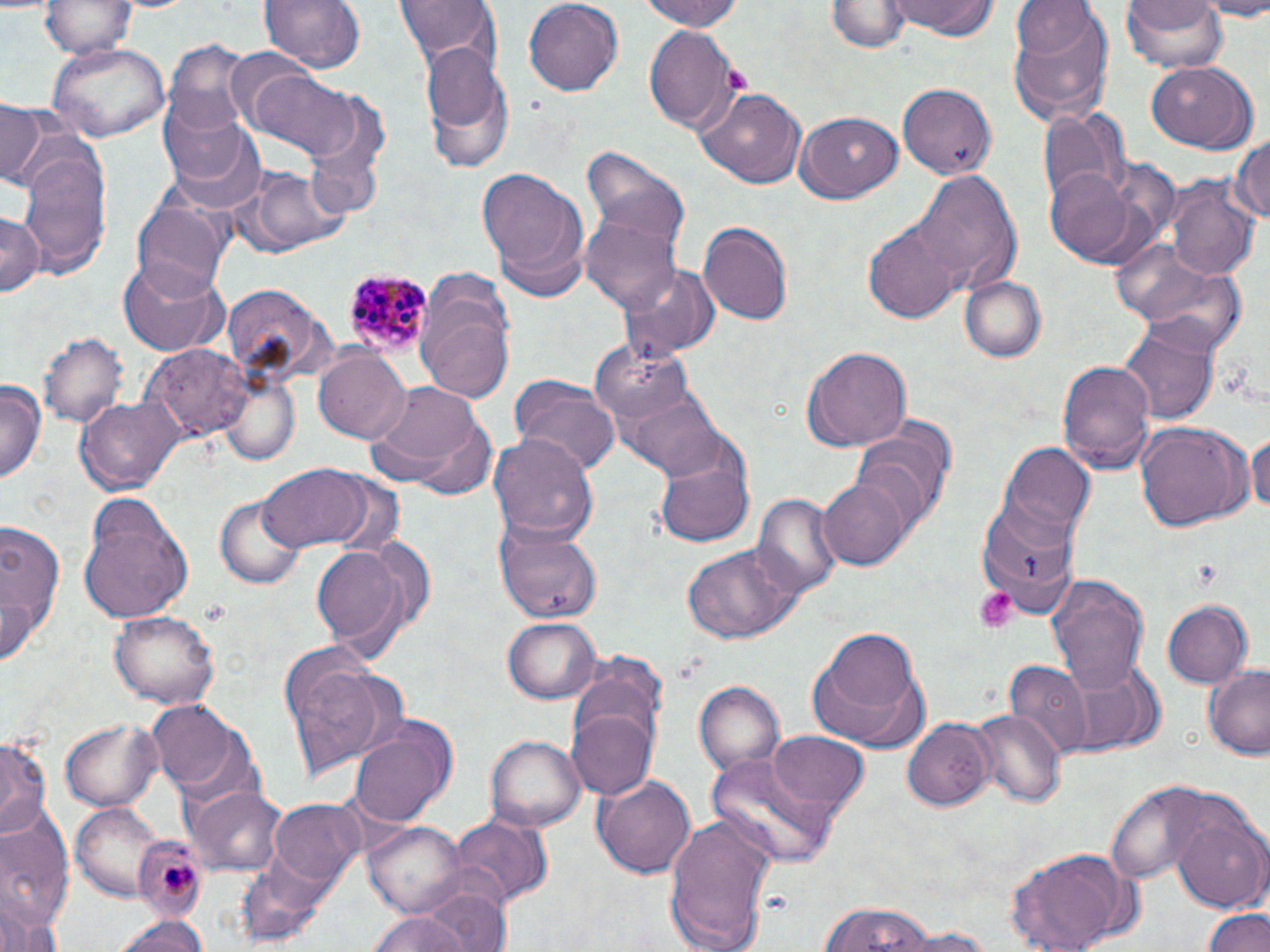

Approximate bounding boxes as named x1/y1/x2/y2 corners in pixels. Platelet locations: (x1=723, y1=66, x2=752, y2=95), (x1=972, y1=586, x2=1018, y2=631), (x1=164, y1=860, x2=196, y2=901). Uninfected red blood cell locations: (x1=258, y1=0, x2=363, y2=76), (x1=394, y1=0, x2=501, y2=73), (x1=521, y1=0, x2=624, y2=96), (x1=643, y1=0, x2=744, y2=31), (x1=829, y1=0, x2=907, y2=54), (x1=887, y1=0, x2=1001, y2=40), (x1=1121, y1=0, x2=1230, y2=75), (x1=1200, y1=0, x2=1270, y2=17), (x1=41, y1=1, x2=137, y2=59), (x1=1008, y1=3, x2=1115, y2=127), (x1=644, y1=23, x2=739, y2=129), (x1=165, y1=41, x2=259, y2=135), (x1=47, y1=42, x2=170, y2=142), (x1=421, y1=45, x2=514, y2=169), (x1=227, y1=48, x2=322, y2=131), (x1=1145, y1=63, x2=1257, y2=152), (x1=239, y1=64, x2=363, y2=159), (x1=899, y1=82, x2=997, y2=180), (x1=699, y1=88, x2=805, y2=188), (x1=157, y1=94, x2=251, y2=186), (x1=1, y1=102, x2=50, y2=187), (x1=1038, y1=105, x2=1132, y2=208), (x1=793, y1=111, x2=902, y2=203), (x1=168, y1=119, x2=267, y2=216), (x1=1231, y1=131, x2=1269, y2=232), (x1=16, y1=142, x2=113, y2=278), (x1=580, y1=148, x2=691, y2=256), (x1=230, y1=165, x2=350, y2=259), (x1=477, y1=166, x2=586, y2=282), (x1=1044, y1=169, x2=1137, y2=264), (x1=913, y1=170, x2=1022, y2=295), (x1=1169, y1=173, x2=1260, y2=283), (x1=133, y1=200, x2=229, y2=299), (x1=0, y1=213, x2=44, y2=298), (x1=579, y1=213, x2=681, y2=312), (x1=699, y1=223, x2=792, y2=325), (x1=864, y1=224, x2=961, y2=321), (x1=1105, y1=239, x2=1226, y2=330), (x1=118, y1=260, x2=228, y2=355), (x1=620, y1=263, x2=719, y2=360), (x1=1135, y1=266, x2=1247, y2=356), (x1=961, y1=275, x2=1047, y2=362), (x1=416, y1=280, x2=516, y2=407), (x1=224, y1=285, x2=324, y2=377), (x1=1118, y1=318, x2=1217, y2=425), (x1=39, y1=331, x2=127, y2=429), (x1=584, y1=338, x2=695, y2=425), (x1=147, y1=343, x2=251, y2=444), (x1=802, y1=347, x2=912, y2=452), (x1=312, y1=348, x2=409, y2=443), (x1=1057, y1=357, x2=1153, y2=472), (x1=218, y1=375, x2=298, y2=465), (x1=511, y1=375, x2=619, y2=476), (x1=0, y1=380, x2=45, y2=486), (x1=615, y1=380, x2=726, y2=477), (x1=363, y1=383, x2=492, y2=496), (x1=79, y1=394, x2=185, y2=493), (x1=852, y1=421, x2=955, y2=528), (x1=1133, y1=423, x2=1251, y2=533), (x1=1248, y1=425, x2=1270, y2=525), (x1=490, y1=432, x2=596, y2=545), (x1=653, y1=438, x2=756, y2=550), (x1=998, y1=442, x2=1095, y2=547), (x1=255, y1=465, x2=387, y2=553), (x1=818, y1=474, x2=908, y2=569), (x1=754, y1=493, x2=842, y2=600), (x1=76, y1=495, x2=193, y2=622), (x1=215, y1=496, x2=304, y2=590), (x1=974, y1=502, x2=1080, y2=613), (x1=0, y1=516, x2=65, y2=662), (x1=493, y1=519, x2=603, y2=622), (x1=309, y1=537, x2=418, y2=659), (x1=680, y1=542, x2=807, y2=645), (x1=1046, y1=574, x2=1149, y2=689), (x1=1162, y1=601, x2=1251, y2=689), (x1=107, y1=610, x2=218, y2=709), (x1=504, y1=616, x2=598, y2=702), (x1=807, y1=628, x2=928, y2=753), (x1=276, y1=644, x2=400, y2=784), (x1=1056, y1=657, x2=1154, y2=756), (x1=1005, y1=661, x2=1091, y2=762), (x1=1203, y1=665, x2=1270, y2=759), (x1=694, y1=682, x2=784, y2=775), (x1=150, y1=700, x2=247, y2=793), (x1=567, y1=703, x2=657, y2=804), (x1=972, y1=708, x2=1065, y2=810), (x1=900, y1=716, x2=994, y2=812), (x1=61, y1=720, x2=164, y2=810), (x1=347, y1=720, x2=455, y2=828), (x1=484, y1=732, x2=585, y2=830), (x1=768, y1=732, x2=868, y2=815), (x1=0, y1=737, x2=50, y2=835), (x1=705, y1=749, x2=840, y2=867), (x1=593, y1=773, x2=696, y2=879), (x1=1106, y1=781, x2=1207, y2=885), (x1=188, y1=782, x2=287, y2=876), (x1=269, y1=800, x2=364, y2=891), (x1=71, y1=801, x2=162, y2=897), (x1=1171, y1=806, x2=1270, y2=911), (x1=660, y1=814, x2=776, y2=952), (x1=446, y1=816, x2=550, y2=910), (x1=0, y1=822, x2=75, y2=934), (x1=366, y1=822, x2=466, y2=919), (x1=129, y1=824, x2=215, y2=920), (x1=1006, y1=843, x2=1134, y2=952), (x1=414, y1=883, x2=515, y2=952), (x1=814, y1=902, x2=937, y2=952), (x1=363, y1=907, x2=483, y2=952), (x1=1203, y1=907, x2=1270, y2=952), (x1=111, y1=913, x2=211, y2=952), (x1=894, y1=928, x2=1001, y2=951). Plasmodium malariae-infected red blood cell locations: (x1=341, y1=268, x2=432, y2=357). Slide-level diagnosis: Plasmodium malariae. Thin blood film. May-Grünwald-Giemsa-stained preparation. Image is 1270×952 pixels. Captured at 1000x magnification. One field of a larger specimen. Light microscopy.